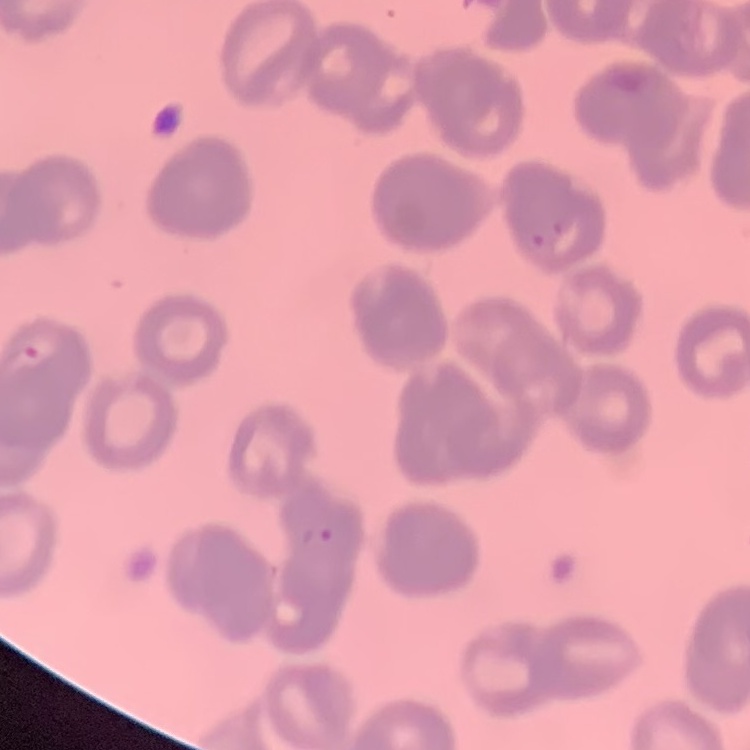
The red blood cells show rouleaux formation. Stained with either Field's or Giemsa. Thin blood film. Square crop of a larger photomicrograph.